Locate every Plasmodium parasite.
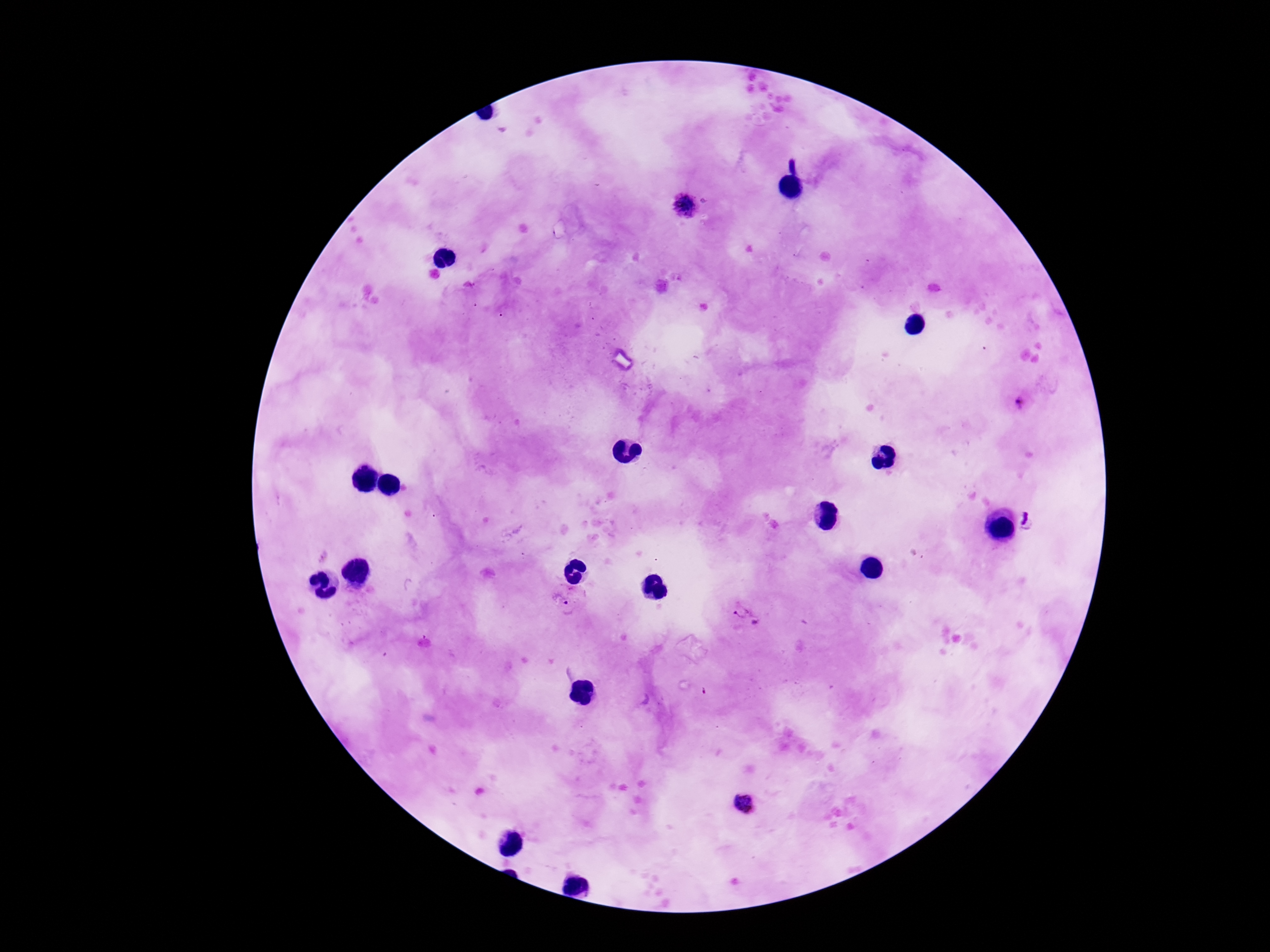

Approximate centers as [x, y] in pixels.
Plasmodium parasites: [684, 209], [1018, 403], [565, 603], [746, 616], [744, 805].

Patient malaria status: positive. Smartphone photograph taken through the microscope eyepiece. Image is 1270×952 pixels. One field from this slide. Thick peripheral-blood smear. 100x magnification. Giemsa stain.